Outline each blood parasite and name the species.
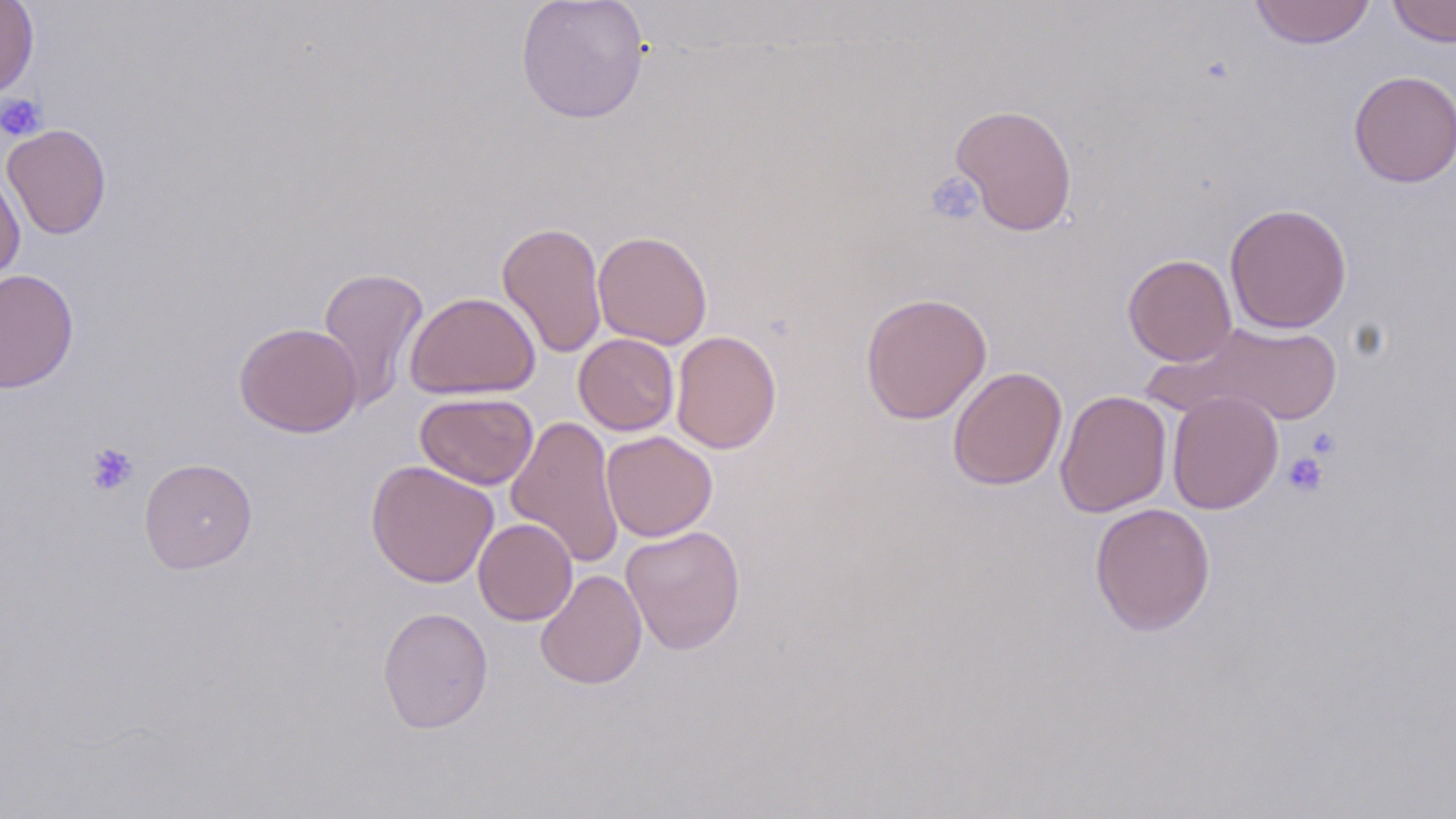
No blood parasites seen.

Summary:
  - Coordinate format: approximate bounding boxes as (x1, y1, x2, y2) in pixels
  - Platelet locations: (0, 93, 47, 141), (925, 171, 984, 226), (1306, 426, 1342, 459), (84, 441, 139, 495), (1283, 451, 1328, 497)
  - Uninfected red blood cell locations: (0, 0, 38, 100), (515, 0, 651, 124), (1249, 0, 1376, 49), (1387, 0, 1456, 47), (1348, 70, 1456, 187), (950, 103, 1078, 236), (2, 123, 112, 239), (0, 169, 25, 283), (1224, 203, 1352, 333), (497, 220, 608, 359), (593, 230, 713, 349), (1123, 253, 1237, 366), (317, 266, 429, 410), (0, 268, 79, 393), (404, 291, 540, 399), (860, 291, 992, 424), (234, 321, 363, 437), (1156, 321, 1345, 427), (671, 330, 782, 454), (574, 333, 679, 436), (947, 366, 1068, 491), (1055, 390, 1172, 517), (1167, 391, 1284, 515), (415, 392, 538, 490), (505, 415, 625, 569), (601, 431, 717, 542), (139, 458, 257, 574), (366, 460, 499, 587), (1090, 502, 1216, 636), (473, 517, 577, 625), (621, 524, 745, 655), (535, 568, 647, 690), (377, 606, 493, 733)
  - Slide-level diagnosis: negative for blood parasites
  - Image size: 1456×819 pixels
  - Stain: May-Grünwald-Giemsa
  - Preparation: thin blood smear
  - Field of view: one of a larger specimen
  - Magnification: 1000x
  - Modality: optical microscopy